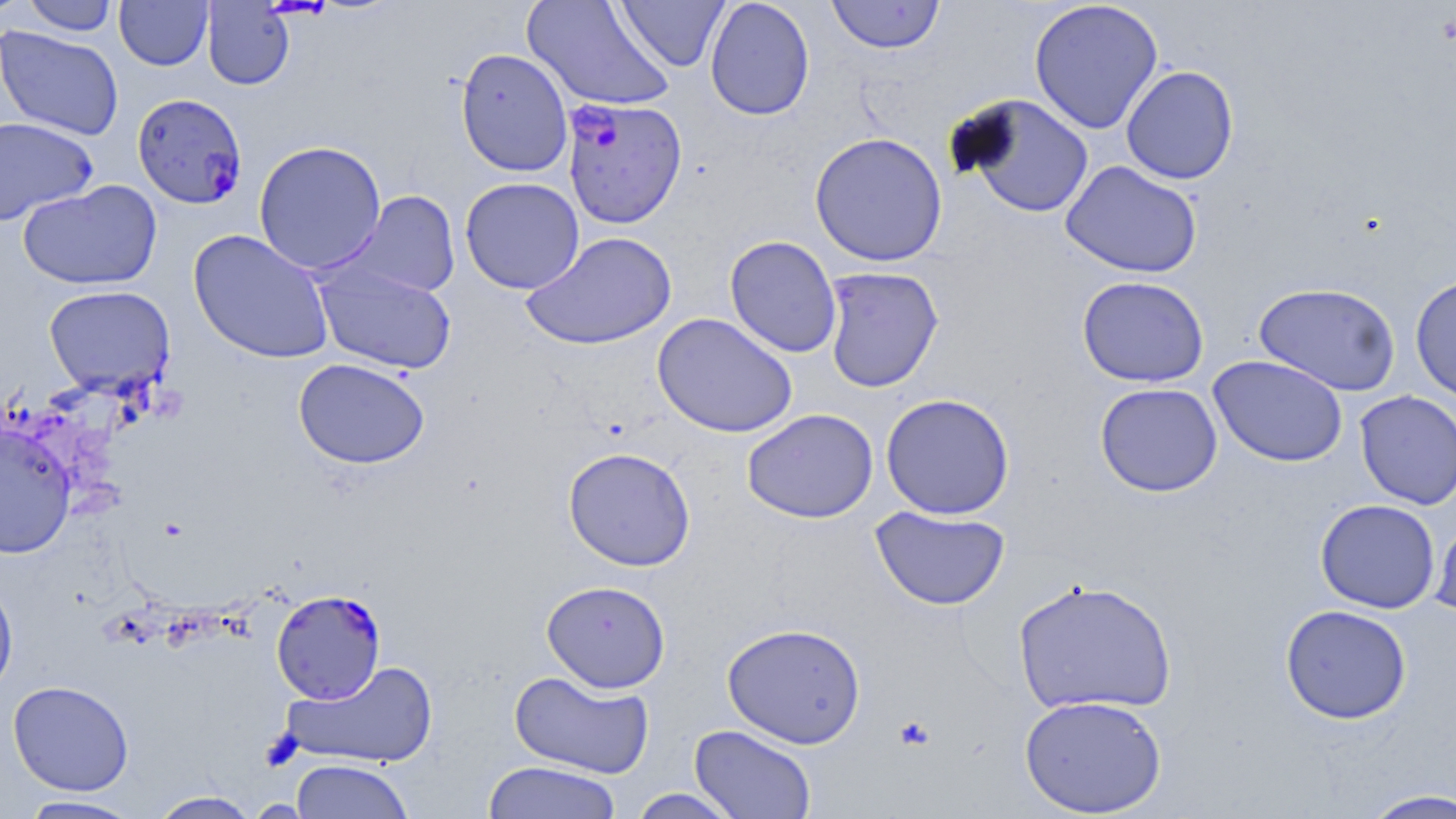

slide-level diagnosis = Plasmodium falciparum
uninfected red blood cell locations = approximate bounding boxes as (x1, y1, x2, y2) in pixels: (0, 0, 30, 21), (22, 0, 119, 36), (114, 0, 213, 70), (522, 0, 676, 112), (614, 0, 730, 72), (704, 0, 815, 121), (826, 0, 945, 54), (1028, 0, 1164, 134), (201, 1, 294, 90), (0, 26, 125, 141), (455, 47, 573, 177), (1121, 65, 1239, 185), (959, 95, 1094, 217), (0, 116, 98, 226), (809, 131, 948, 267), (253, 140, 387, 275), (1060, 160, 1203, 279), (460, 177, 585, 295), (18, 180, 162, 291), (340, 190, 461, 299), (188, 229, 335, 364), (521, 230, 678, 350), (724, 235, 843, 358), (314, 263, 457, 375), (821, 266, 944, 393), (1409, 274, 1456, 405), (1077, 275, 1209, 387), (1253, 282, 1402, 397), (43, 285, 176, 396), (652, 312, 798, 438), (1208, 355, 1348, 467), (293, 358, 430, 469), (1095, 382, 1223, 497), (1355, 390, 1455, 509), (880, 392, 1015, 520), (742, 408, 878, 523), (0, 422, 76, 560), (562, 446, 696, 571), (1315, 499, 1440, 613), (870, 506, 1011, 610), (1430, 511, 1456, 622), (0, 574, 19, 699), (1013, 578, 1178, 717), (541, 579, 671, 693), (1280, 604, 1412, 724), (721, 622, 867, 749), (281, 659, 438, 769), (508, 669, 655, 778), (8, 681, 134, 796), (1019, 694, 1167, 816), (689, 724, 817, 819), (290, 759, 415, 818), (482, 760, 623, 819), (627, 788, 743, 818), (1357, 788, 1456, 818), (146, 790, 263, 818), (15, 795, 145, 818)
magnification = 1000x
modality = light microscopy
stain = May-Grünwald-Giemsa
field of view = single
Plasmodium falciparum-infected red blood cell locations = approximate bounding boxes as (x1, y1, x2, y2) in pixels: (132, 91, 251, 209), (561, 97, 687, 228), (272, 590, 386, 703)
platelet locations = approximate bounding boxes as (x1, y1, x2, y2) in pixels: (894, 715, 936, 751)
image size = 1456×819 pixels
preparation = thin blood film